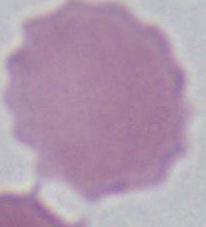
modality: micrograph
identification: erythrocyte
magnification: 1000x